Locate every blood parasite and identify its species.
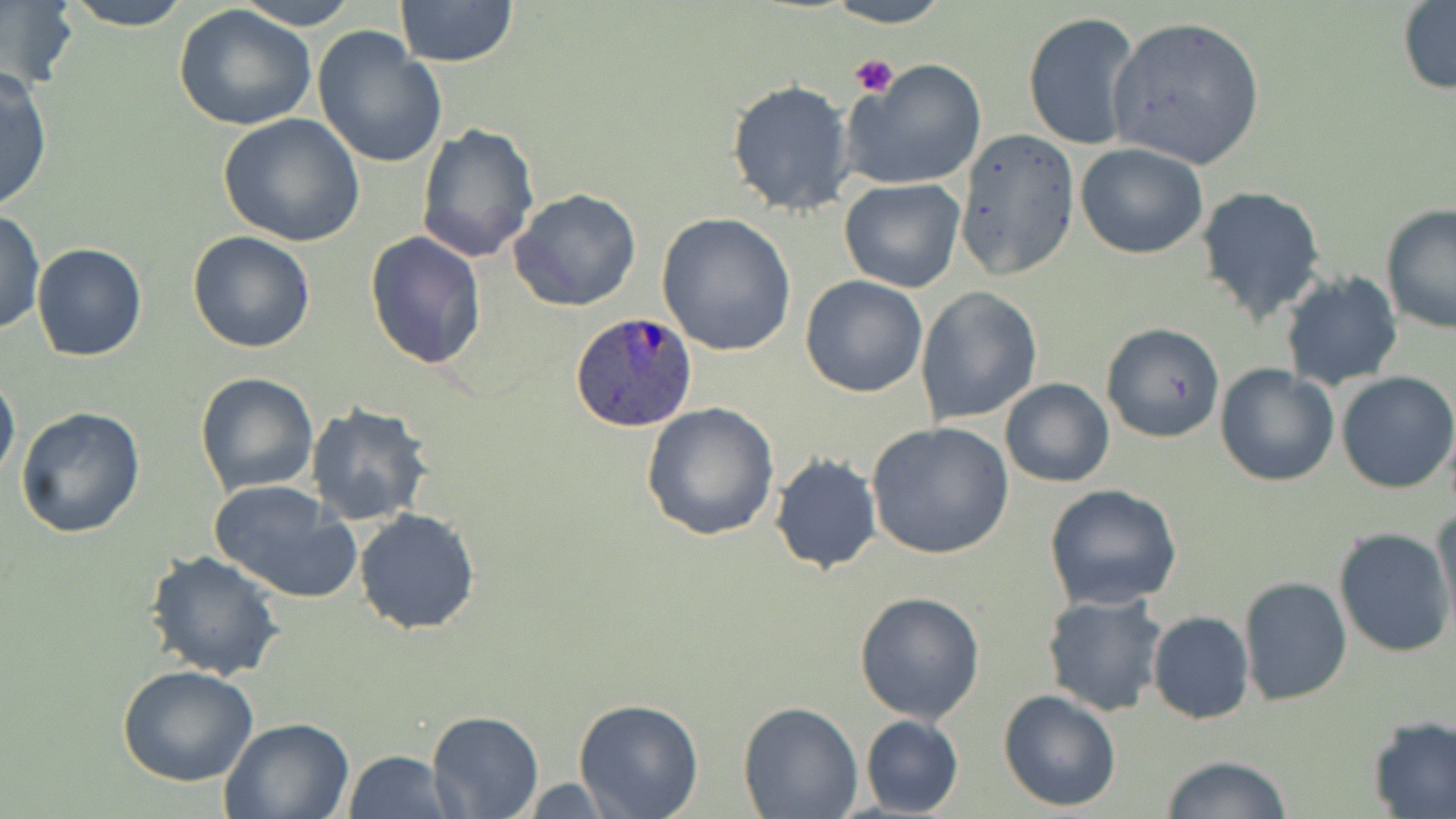
Approximate bounding boxes as [x1, y1, x2, y2] in pixels.
Plasmodium ovale-infected red blood cells: [570, 311, 701, 433].
No Plasmodium falciparum, Plasmodium malariae, Plasmodium vivax, Babesia divergens, or Trypanosoma brucei observed.

Summary:
  - Platelet locations: [850, 54, 900, 98]
  - Uninfected red blood cell locations: [61, 0, 194, 31], [233, 0, 361, 30], [393, 0, 519, 67], [825, 0, 951, 28], [1397, 1, 1456, 96], [2, 2, 77, 91], [173, 5, 317, 133], [1023, 11, 1144, 154], [1106, 15, 1266, 170], [312, 27, 448, 171], [847, 58, 990, 189], [0, 67, 54, 213], [726, 78, 855, 216], [219, 113, 367, 248], [416, 122, 540, 265], [953, 126, 1079, 280], [1075, 142, 1208, 259], [840, 178, 966, 293], [1197, 185, 1328, 326], [509, 189, 643, 312], [1379, 203, 1455, 334], [1, 209, 45, 334], [656, 211, 798, 357], [186, 230, 316, 354], [365, 230, 488, 371], [32, 242, 146, 361], [1278, 270, 1403, 391], [799, 274, 928, 397], [914, 286, 1043, 425], [1101, 321, 1225, 445], [1215, 365, 1340, 487], [0, 369, 20, 485], [194, 371, 320, 495], [1336, 372, 1456, 493], [1000, 378, 1115, 487], [641, 402, 781, 541], [303, 403, 436, 529], [16, 407, 146, 540], [866, 420, 1014, 561], [769, 453, 882, 574], [209, 479, 362, 604], [1044, 484, 1185, 610], [1433, 504, 1456, 632], [354, 508, 481, 635], [1333, 527, 1455, 659], [145, 549, 286, 682], [1238, 576, 1354, 707], [853, 590, 985, 723], [1042, 593, 1168, 716], [1147, 611, 1254, 724], [117, 665, 260, 787], [998, 689, 1123, 812], [573, 698, 704, 819], [737, 700, 864, 818], [428, 708, 543, 817], [860, 715, 964, 817], [1367, 715, 1456, 818], [219, 717, 353, 819], [343, 751, 454, 819], [1160, 755, 1295, 818], [507, 777, 627, 815]
  - Slide-level diagnosis: Plasmodium ovale
  - Preparation: thin blood film
  - Image size: 1456×819 pixels
  - Field of view: one of a larger specimen
  - Magnification: 1000x
  - Stain: May-Grünwald-Giemsa
  - Modality: light microscopy